Assess this cell for malaria.
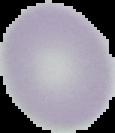
It is uninfected.

preparation = thin blood film
image size = 115×133 pixels
image type = segmented cell region with the area outside set to black